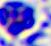

modality = photomicrograph
magnification = 400x
identification = white blood cell